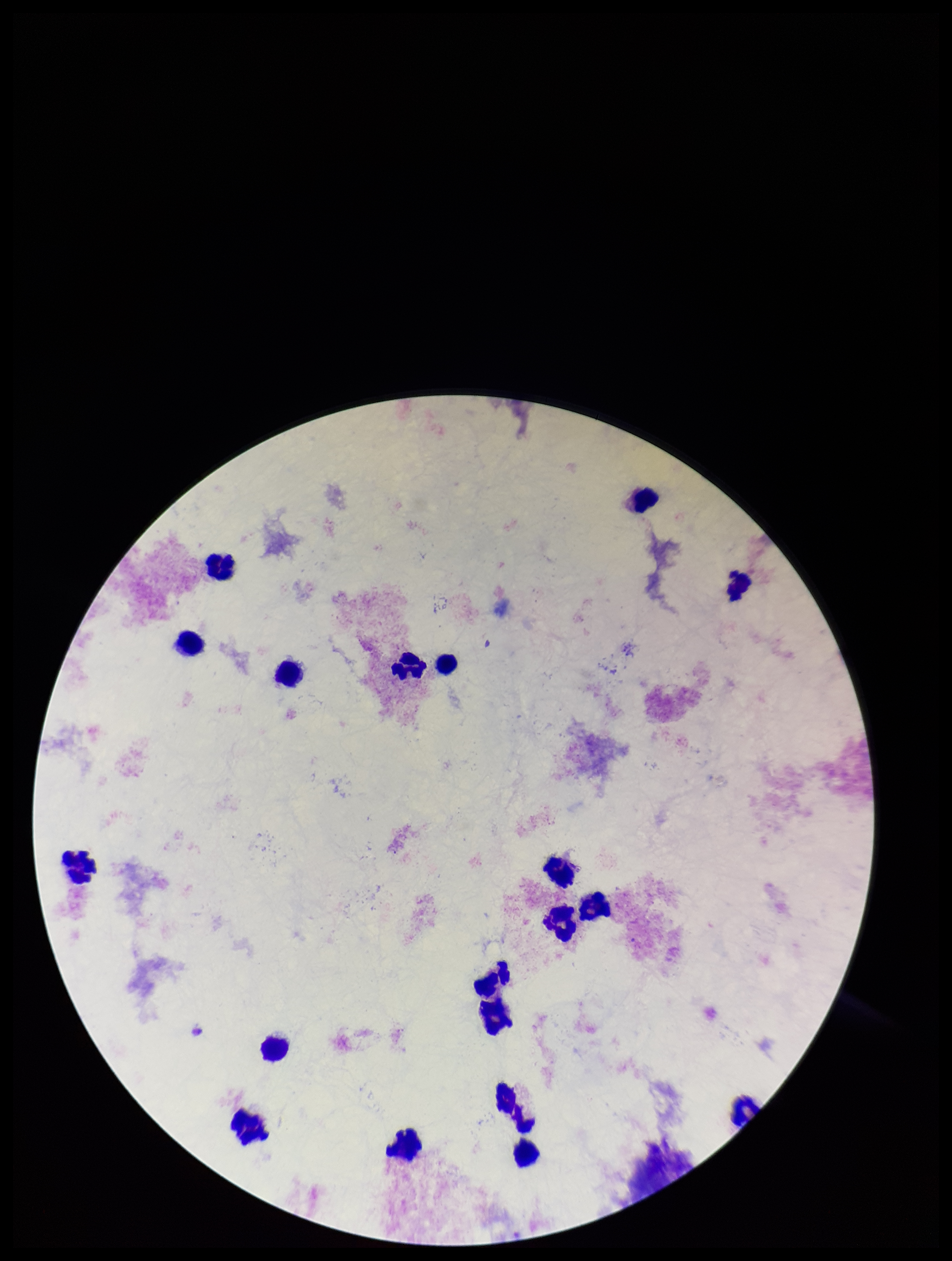

Patient malaria status: negative. Preparation: thick smear. Plasmodium parasites: none identified. Image is 952×1261 pixels. Stained with Giemsa. Single field of view. Parasite count: 0. Leukocyte count: 18. Smartphone photograph taken through the eyepiece of a microscope.